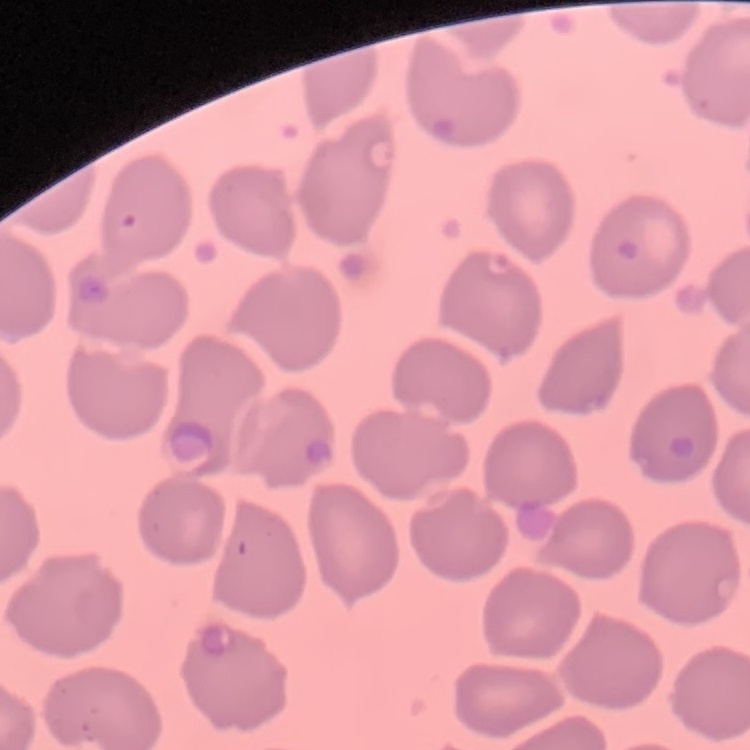

The erythrocytes show no rouleaux formation. Square crop of a larger photomicrograph. Thin peripheral smear. Field's or Giemsa stain.